Name the parasite shown.
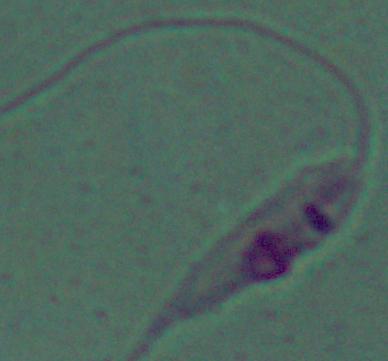

This is Leishmania.

magnification: 1000x
modality: photomicrograph